Describe the morphology of the erythrocytes.
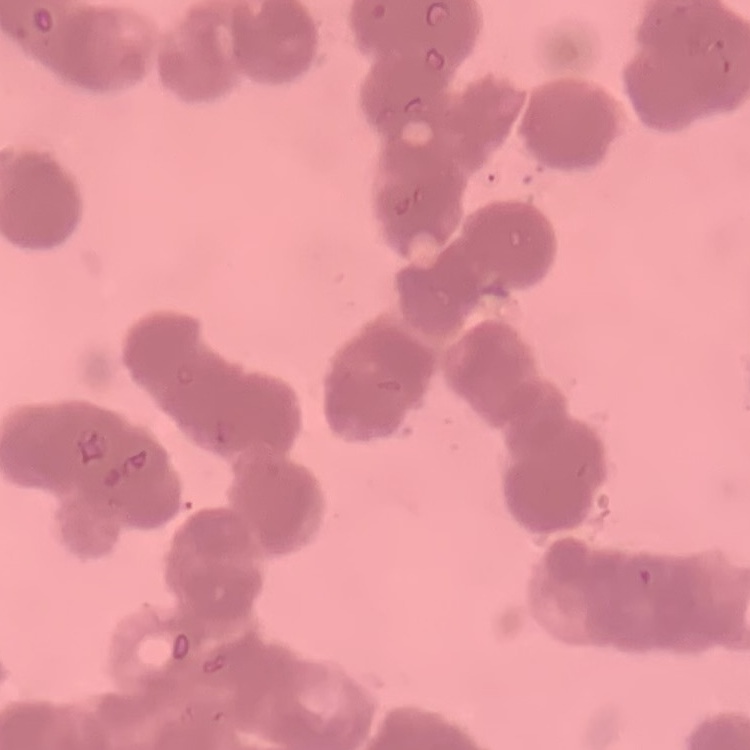

They show rouleaux formation.

Summary:
  - Preparation: thin peripheral smear
  - Image type: square crop of a larger photomicrograph
  - Stain: Field's or Giemsa